Classify this cell by malaria status.
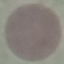

It is uninfected.

image type = cell patch, automatically extracted from a larger field of view and resized to 64 × 64 pixels
preparation = thin blood film
stain = Giemsa
capture = smartphone through the microscope eyepiece